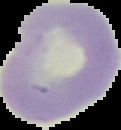
Summary:
  - Preparation: thin blood film
  - Malaria status: uninfected
  - Image type: cell region segmented out of the field of view; surrounding area masked to black
  - Image size: 121×130 pixels